Assess this cell for malaria.
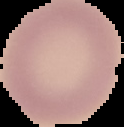

Uninfected.

preparation = thin blood smear
image size = 124×127 pixels
image type = segmented cell region on a black background